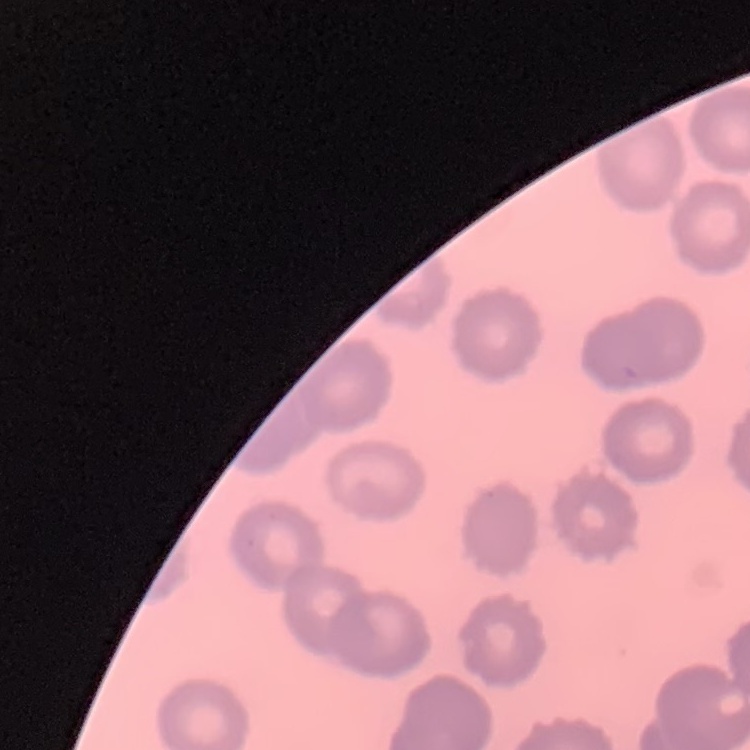

{
  "red_blood_cell_morphology": "no rouleaux formation",
  "stain": "Field's or Giemsa",
  "preparation": "thin peripheral smear",
  "image_type": "square crop of a larger photomicrograph"
}